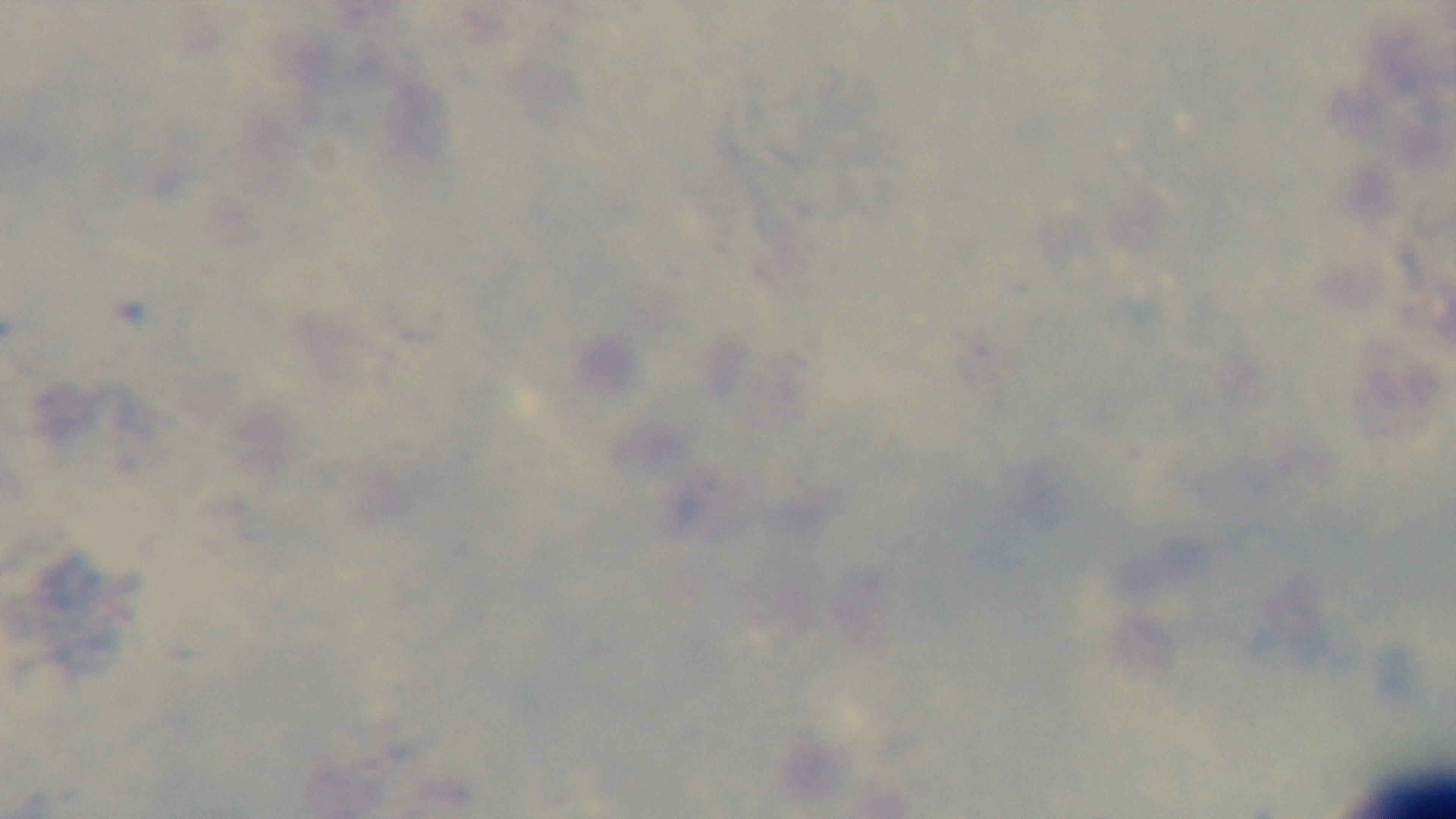
Summary:
  - Preparation: thick blood film
  - Modality: light microscopy
  - Stain: Giemsa
  - Malaria status: uninfected
  - Objective: 100x oil immersion
  - Capture: mounted 4K digital camera
  - Field of view: one from the slide